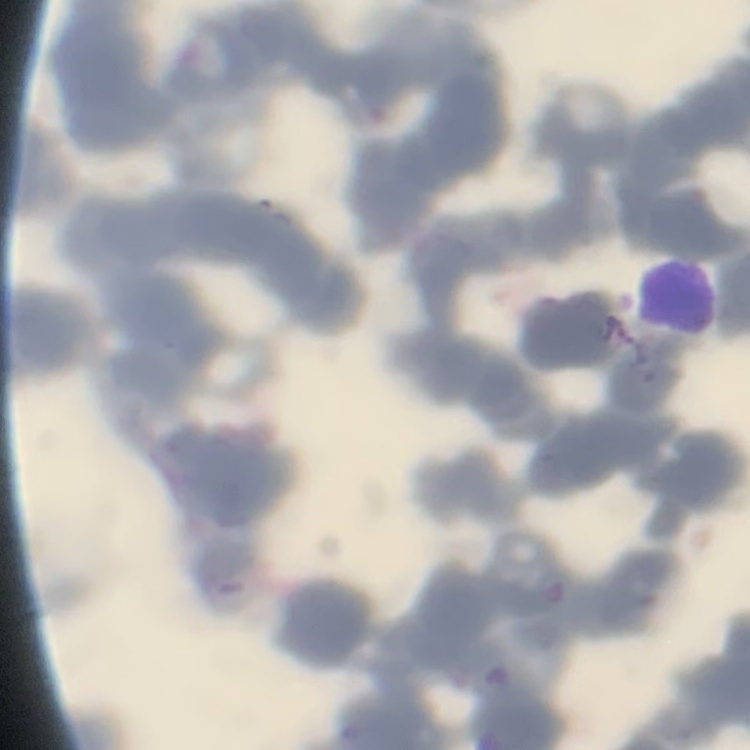 The erythrocytes exhibit rouleaux formation. One tile cut from a larger photomicrograph. Stained with either Field's or Giemsa. Thin peripheral smear.